Assess this cell for malaria.
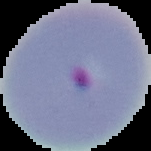
It is parasitized.

preparation = thin blood film
image size = 151×151 pixels
image type = cell region segmented out of the field of view; surrounding area masked to black